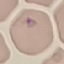
malaria status = parasitized
capture = smartphone through the microscope eyepiece
preparation = thin blood film
stain = Giemsa
image type = cell patch, automatically extracted from a larger field of view and resized to 64 × 64 pixels